Report the malaria status of this cell.
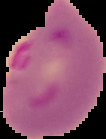

It is parasitized.

From a thin blood smear. Segmented cell region on a black background. Image is 106×139 pixels.